Classify this cell by malaria status.
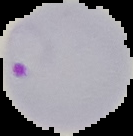
It is parasitized.

Summary:
  - Preparation: thin blood film
  - Image size: 133×136 pixels
  - Image type: segmented cell region on a black background